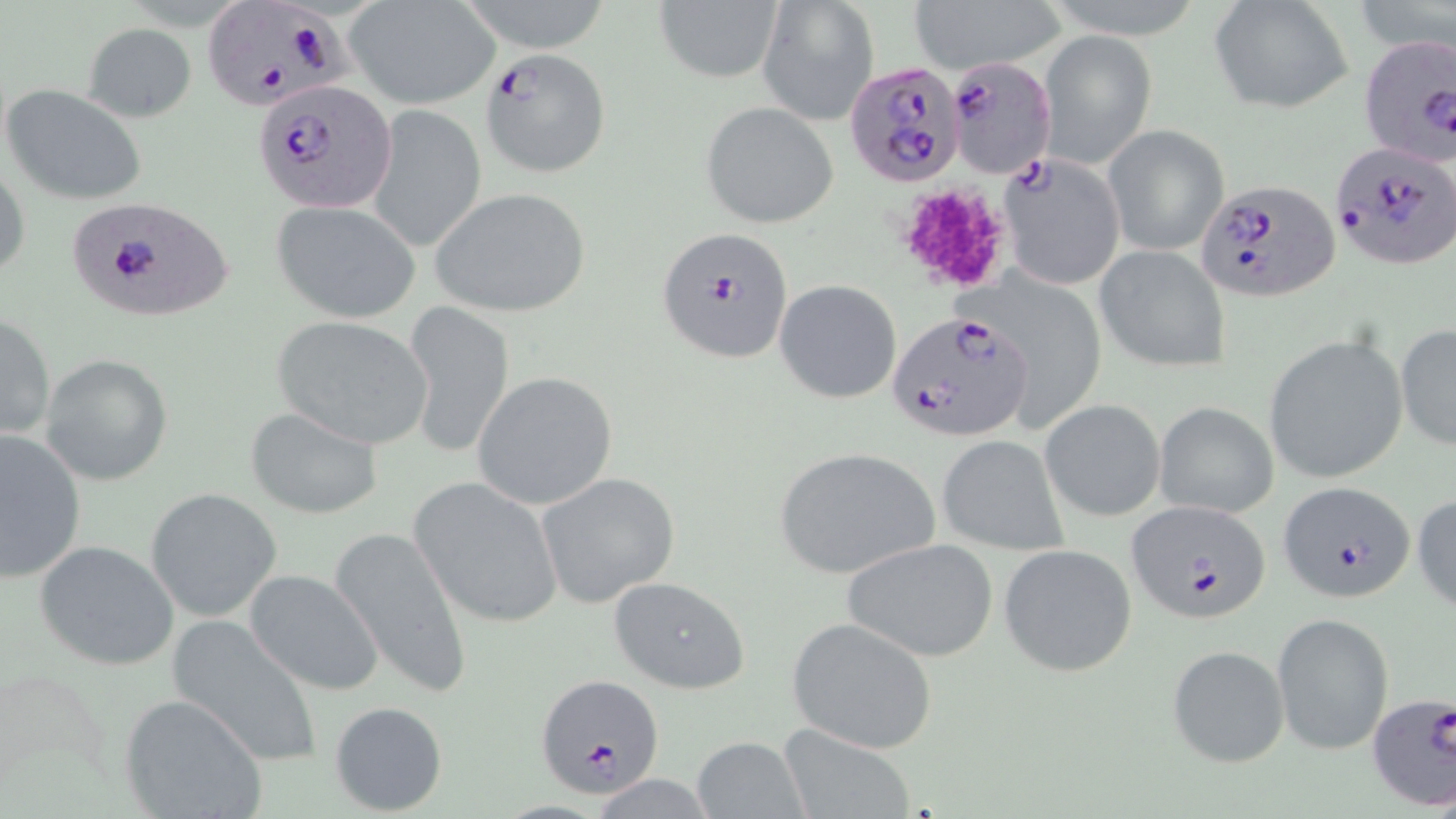
{
  "slide_level_diagnosis": "Plasmodium falciparum",
  "platelet_locations": "approximate bounding boxes as [x1, y1, x2, y2] in pixels: [892, 181, 1016, 294]",
  "magnification": "1000x",
  "preparation": "thin blood smear",
  "uninfected_red_blood_cell_locations": "approximate bounding boxes as [x1, y1, x2, y2] in pixels: [456, 0, 618, 54], [906, 0, 1069, 71], [1208, 0, 1354, 116], [654, 1, 782, 83], [758, 1, 877, 126], [346, 2, 498, 110], [83, 23, 196, 121], [1038, 29, 1157, 171], [4, 84, 149, 206], [702, 102, 839, 229], [370, 105, 487, 254], [1102, 124, 1230, 256], [0, 158, 31, 287], [428, 187, 592, 316], [272, 198, 419, 321], [1095, 245, 1232, 373], [776, 280, 900, 403], [402, 303, 514, 460], [0, 312, 54, 443], [272, 316, 433, 449], [1395, 323, 1455, 451], [1265, 334, 1409, 484], [41, 354, 173, 485], [471, 371, 618, 510], [1040, 398, 1165, 522], [1154, 400, 1278, 518], [244, 406, 384, 520], [0, 429, 87, 584], [935, 435, 1066, 555], [771, 447, 939, 580], [535, 472, 679, 607], [409, 475, 564, 629], [144, 487, 282, 621], [1413, 488, 1456, 617], [328, 523, 475, 700], [841, 537, 1000, 664], [35, 540, 180, 671], [996, 542, 1137, 676], [244, 568, 384, 694], [608, 576, 751, 693], [1272, 613, 1394, 756], [166, 615, 327, 769], [788, 618, 937, 752], [1164, 644, 1290, 769], [118, 693, 267, 819], [330, 700, 449, 815], [775, 725, 917, 819], [691, 735, 808, 817]",
  "stain": "May-Grünwald-Giemsa",
  "image_size": "1456×819 pixels",
  "field_of_view": "single",
  "plasmodium_falciparum_infected_red_blood_cell_locations": "approximate bounding boxes as [x1, y1, x2, y2] in pixels: [208, 4, 358, 105], [1356, 35, 1456, 168], [480, 50, 611, 179], [844, 59, 969, 191], [940, 59, 1062, 178], [254, 80, 395, 214], [1329, 141, 1455, 271], [998, 153, 1125, 290], [1196, 177, 1339, 301], [64, 195, 234, 323], [654, 224, 794, 365], [887, 311, 1033, 442], [1278, 480, 1417, 604], [1126, 500, 1272, 625], [541, 681, 669, 806], [1365, 694, 1455, 809]",
  "modality": "light microscopy"
}